Identify the blood parasite species.
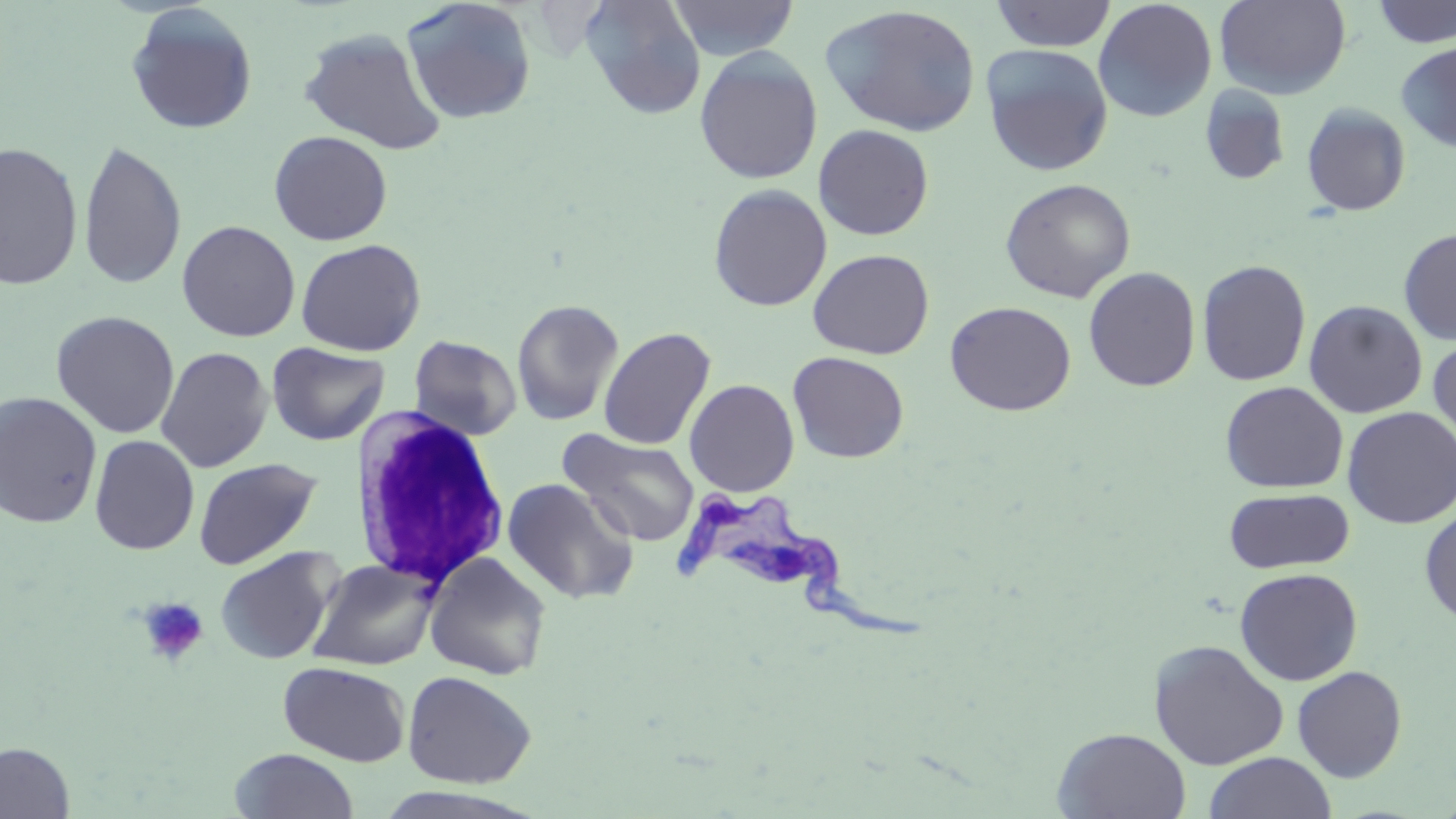
Trypanosoma brucei.

Summary:
  - Coordinate format: approximate bounding boxes as named x1/y1/x2/y2 corners in pixels
  - Platelet locations: (x1=137, y1=596, x2=209, y2=667)
  - Trypanosoma brucei locations: (x1=676, y1=489, x2=927, y2=646)
  - Uninfected red blood cell locations: (x1=580, y1=0, x2=706, y2=119), (x1=667, y1=0, x2=800, y2=61), (x1=990, y1=0, x2=1117, y2=52), (x1=1215, y1=0, x2=1351, y2=100), (x1=401, y1=1, x2=537, y2=124), (x1=1093, y1=1, x2=1217, y2=123), (x1=1371, y1=1, x2=1456, y2=48), (x1=820, y1=4, x2=981, y2=137), (x1=125, y1=5, x2=258, y2=135), (x1=299, y1=26, x2=448, y2=155), (x1=1395, y1=41, x2=1456, y2=153), (x1=980, y1=44, x2=1113, y2=176), (x1=694, y1=48, x2=823, y2=185), (x1=1200, y1=84, x2=1291, y2=186), (x1=1301, y1=103, x2=1411, y2=216), (x1=813, y1=124, x2=934, y2=241), (x1=268, y1=130, x2=392, y2=246), (x1=284, y1=131, x2=404, y2=357), (x1=77, y1=140, x2=187, y2=290), (x1=0, y1=142, x2=83, y2=291), (x1=1000, y1=178, x2=1136, y2=303), (x1=708, y1=183, x2=832, y2=312), (x1=177, y1=220, x2=300, y2=342), (x1=1398, y1=227, x2=1456, y2=344), (x1=294, y1=238, x2=427, y2=356), (x1=808, y1=249, x2=934, y2=359), (x1=1197, y1=258, x2=1311, y2=387), (x1=1083, y1=266, x2=1201, y2=392), (x1=511, y1=299, x2=624, y2=426), (x1=1304, y1=299, x2=1427, y2=418), (x1=945, y1=301, x2=1076, y2=416), (x1=51, y1=311, x2=180, y2=438), (x1=598, y1=327, x2=716, y2=451), (x1=50, y1=331, x2=273, y2=463), (x1=408, y1=335, x2=522, y2=441), (x1=1428, y1=336, x2=1456, y2=452), (x1=267, y1=342, x2=390, y2=446), (x1=155, y1=346, x2=273, y2=473), (x1=788, y1=352, x2=909, y2=463), (x1=684, y1=379, x2=799, y2=497), (x1=1220, y1=381, x2=1348, y2=494), (x1=0, y1=391, x2=103, y2=529), (x1=1342, y1=406, x2=1456, y2=529), (x1=559, y1=429, x2=701, y2=546), (x1=89, y1=435, x2=199, y2=555), (x1=193, y1=457, x2=322, y2=570), (x1=501, y1=477, x2=639, y2=605), (x1=1223, y1=487, x2=1355, y2=574), (x1=1419, y1=507, x2=1456, y2=626), (x1=215, y1=547, x2=341, y2=665), (x1=424, y1=553, x2=552, y2=681), (x1=307, y1=558, x2=441, y2=671), (x1=1234, y1=568, x2=1363, y2=686), (x1=1149, y1=639, x2=1289, y2=770), (x1=278, y1=661, x2=410, y2=767), (x1=1292, y1=665, x2=1408, y2=782), (x1=402, y1=670, x2=537, y2=789), (x1=1053, y1=727, x2=1192, y2=818), (x1=0, y1=741, x2=76, y2=819), (x1=229, y1=748, x2=358, y2=818), (x1=1203, y1=752, x2=1337, y2=819), (x1=365, y1=786, x2=545, y2=819)
  - White blood cell locations: (x1=347, y1=405, x2=512, y2=591)
  - Preparation: thin blood film
  - Stain: May-Grünwald-Giemsa
  - Image size: 1456×819 pixels
  - Modality: light microscopy
  - Field of view: single
  - Magnification: 1000x